Assess this cell for malaria.
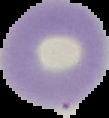
Uninfected.

Summary:
  - Preparation: thin blood film
  - Image size: 109×118 pixels
  - Image type: segmented cell region on a black background